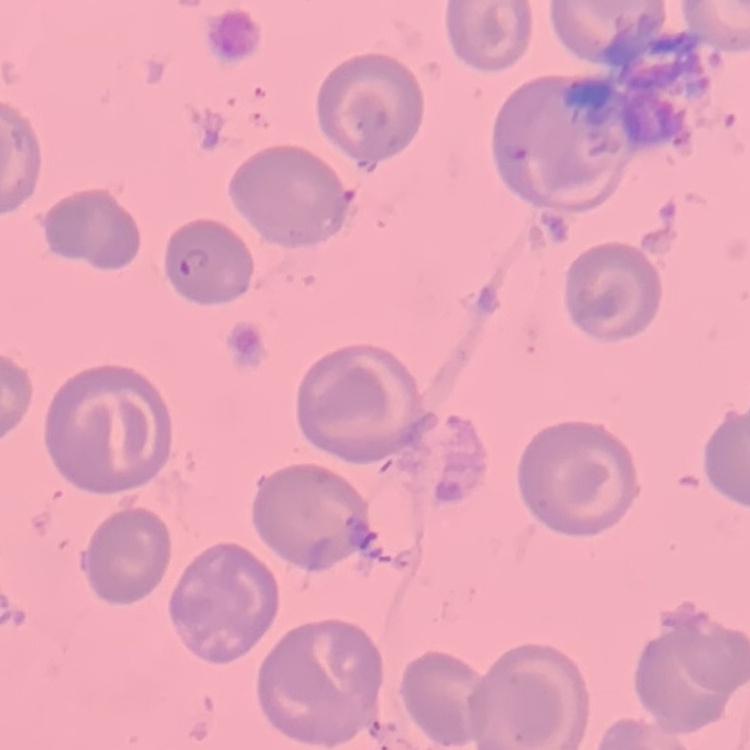

red_blood_cell_morphology: no rouleaux formation
preparation: thin peripheral smear
stain: Field's or Giemsa
image_type: one tile cut from a larger photomicrograph